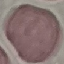
malaria status = uninfected
preparation = thin smear
image type = cell patch, automatically extracted from a larger field of view and resized to 64 × 64 pixels
capture = smartphone camera at the microscope eyepiece
stain = Giemsa